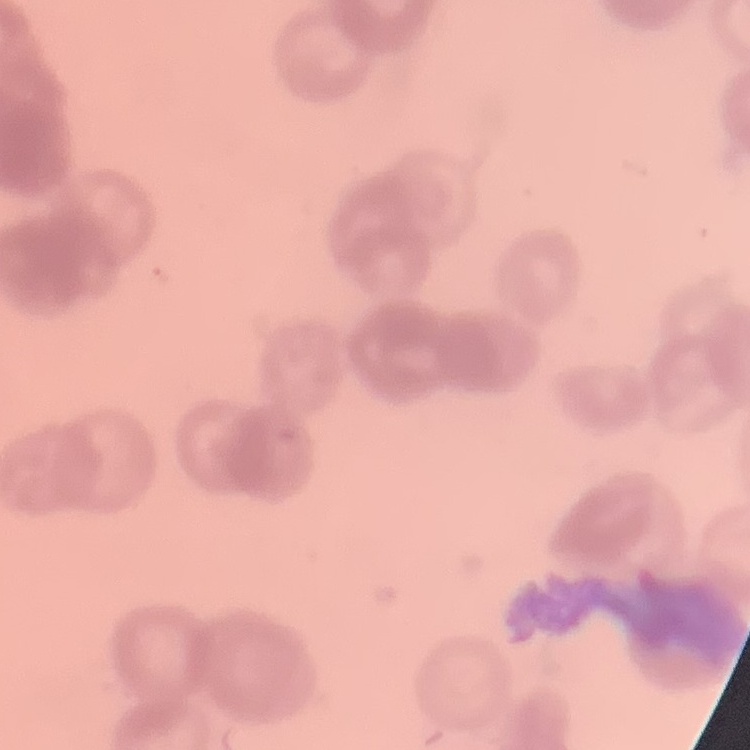

erythrocyte morphology = rouleaux formation
preparation = thin peripheral smear
stain = Field's or Giemsa
image type = one tile cut from a larger photomicrograph